State which parasite is depicted.
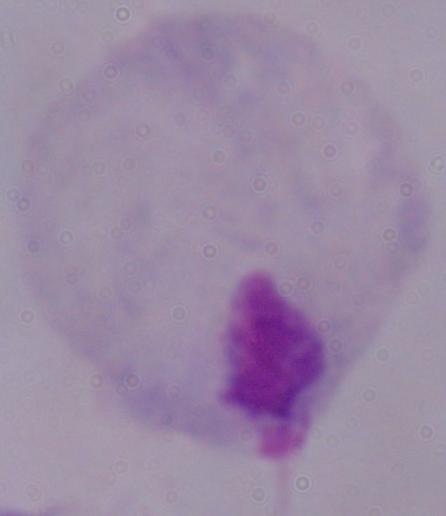
A trichomonad.

Summary:
  - Modality: photomicrograph
  - Magnification: 1000x